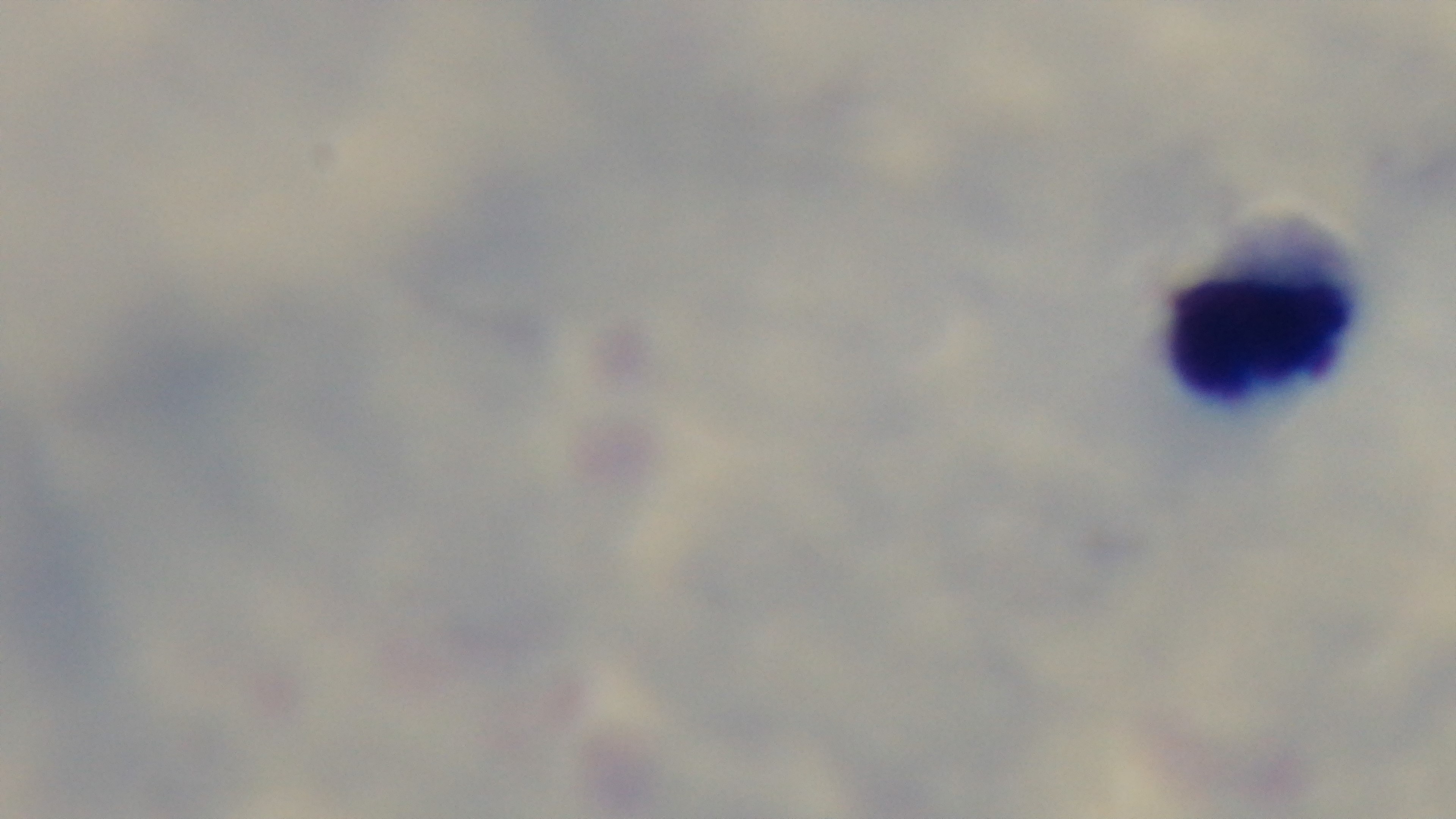

Preparation: thick. Oil-immersion objective, 100x. Photomicrograph. Mounted 4K digital camera. One field from the slide. Malaria status: negative. Giemsa-stained.